Outline each blood parasite and name the species.
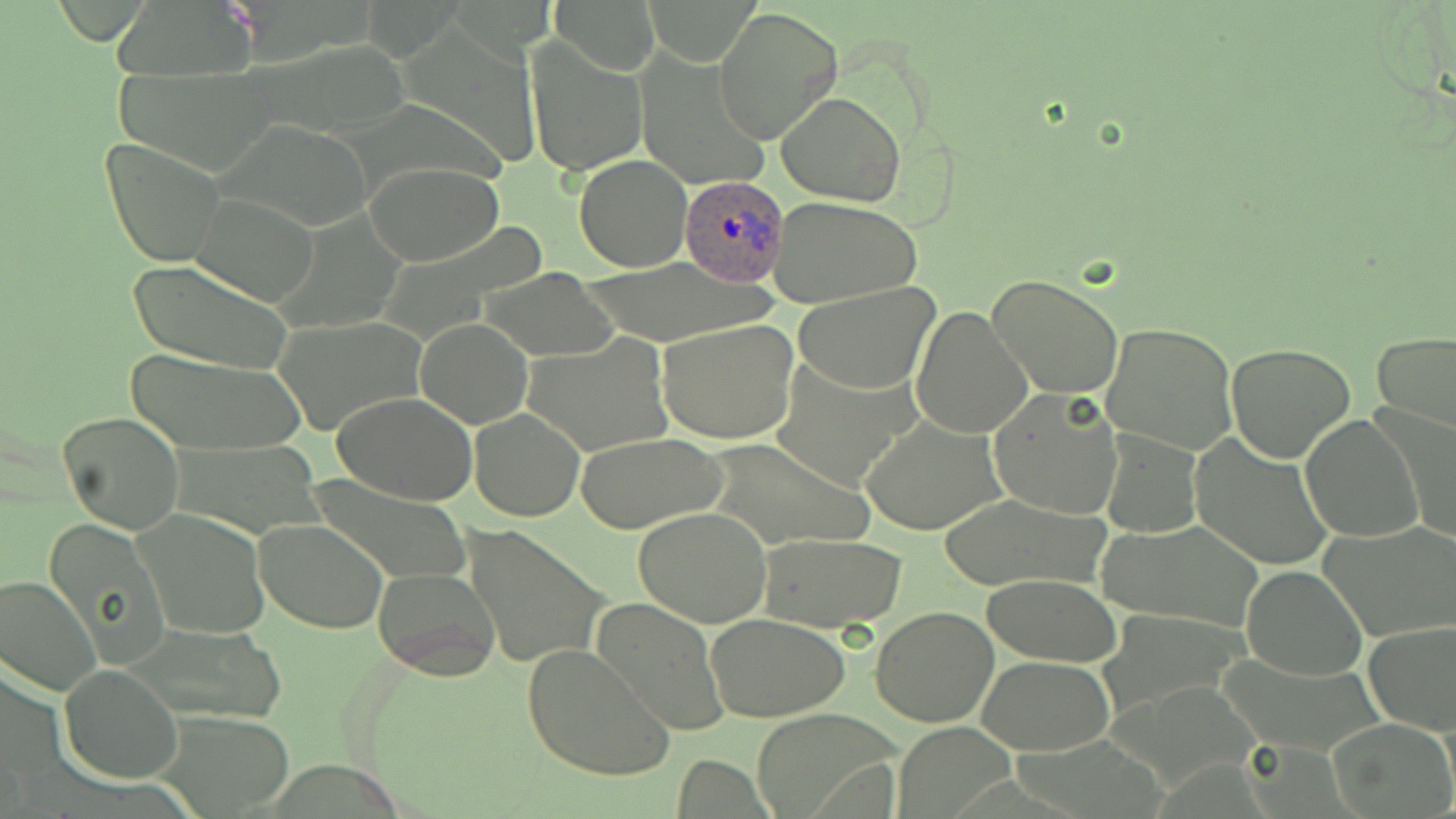

Approximate bounding boxes as named x1/y1/x2/y2 corners in pixels.
Plasmodium ovale-infected red blood cells: (x1=679, y1=176, x2=788, y2=288).
No Plasmodium falciparum, Plasmodium malariae, Plasmodium vivax, Babesia divergens, or Trypanosoma brucei observed.

slide-level diagnosis = Plasmodium ovale
preparation = thin blood smear
modality = optical microscopy
uninfected red blood cell locations = approximate bounding boxes as named x1/y1/x2/y2 corners in pixels: (x1=552, y1=0, x2=659, y2=74), (x1=643, y1=0, x2=763, y2=65), (x1=714, y1=6, x2=843, y2=145), (x1=525, y1=39, x2=649, y2=176), (x1=641, y1=56, x2=770, y2=188), (x1=777, y1=92, x2=906, y2=206), (x1=219, y1=120, x2=377, y2=230), (x1=101, y1=137, x2=229, y2=267), (x1=573, y1=155, x2=691, y2=271), (x1=365, y1=162, x2=504, y2=266), (x1=190, y1=191, x2=321, y2=306), (x1=767, y1=195, x2=921, y2=310), (x1=380, y1=226, x2=543, y2=340), (x1=578, y1=258, x2=775, y2=343), (x1=125, y1=260, x2=296, y2=378), (x1=479, y1=269, x2=616, y2=361), (x1=987, y1=274, x2=1123, y2=397), (x1=792, y1=283, x2=940, y2=395), (x1=911, y1=305, x2=1034, y2=441), (x1=275, y1=317, x2=424, y2=437), (x1=414, y1=318, x2=533, y2=428), (x1=658, y1=319, x2=799, y2=445), (x1=1101, y1=320, x2=1240, y2=455), (x1=1371, y1=329, x2=1456, y2=437), (x1=526, y1=332, x2=674, y2=455), (x1=1225, y1=343, x2=1356, y2=464), (x1=120, y1=347, x2=308, y2=455), (x1=768, y1=354, x2=920, y2=491), (x1=987, y1=386, x2=1125, y2=521), (x1=333, y1=391, x2=479, y2=507), (x1=1373, y1=403, x2=1456, y2=543), (x1=470, y1=408, x2=586, y2=523), (x1=57, y1=411, x2=184, y2=532), (x1=1299, y1=413, x2=1423, y2=544), (x1=859, y1=415, x2=1009, y2=534), (x1=1099, y1=427, x2=1203, y2=538), (x1=574, y1=432, x2=727, y2=533), (x1=1189, y1=434, x2=1334, y2=570), (x1=701, y1=439, x2=872, y2=550), (x1=306, y1=478, x2=473, y2=583), (x1=934, y1=491, x2=1108, y2=593), (x1=134, y1=506, x2=270, y2=638), (x1=633, y1=507, x2=773, y2=627), (x1=43, y1=517, x2=171, y2=670), (x1=252, y1=519, x2=389, y2=635), (x1=1099, y1=519, x2=1263, y2=633), (x1=1321, y1=522, x2=1456, y2=641), (x1=465, y1=525, x2=607, y2=670), (x1=753, y1=531, x2=909, y2=633), (x1=374, y1=564, x2=502, y2=680), (x1=1241, y1=565, x2=1367, y2=680), (x1=0, y1=573, x2=100, y2=696), (x1=980, y1=574, x2=1121, y2=667), (x1=592, y1=598, x2=732, y2=735), (x1=870, y1=605, x2=1000, y2=729), (x1=706, y1=613, x2=850, y2=722), (x1=1364, y1=619, x2=1456, y2=735), (x1=123, y1=625, x2=283, y2=727), (x1=522, y1=642, x2=676, y2=783), (x1=978, y1=655, x2=1112, y2=753), (x1=58, y1=664, x2=183, y2=783), (x1=750, y1=711, x2=896, y2=816), (x1=1329, y1=718, x2=1455, y2=818), (x1=892, y1=722, x2=1016, y2=816)
field of view = single
stain = May-Grünwald-Giemsa
image size = 1456×819 pixels
magnification = 1000x